Locate every P. falciparum parasite and identify its life-cycle stage.
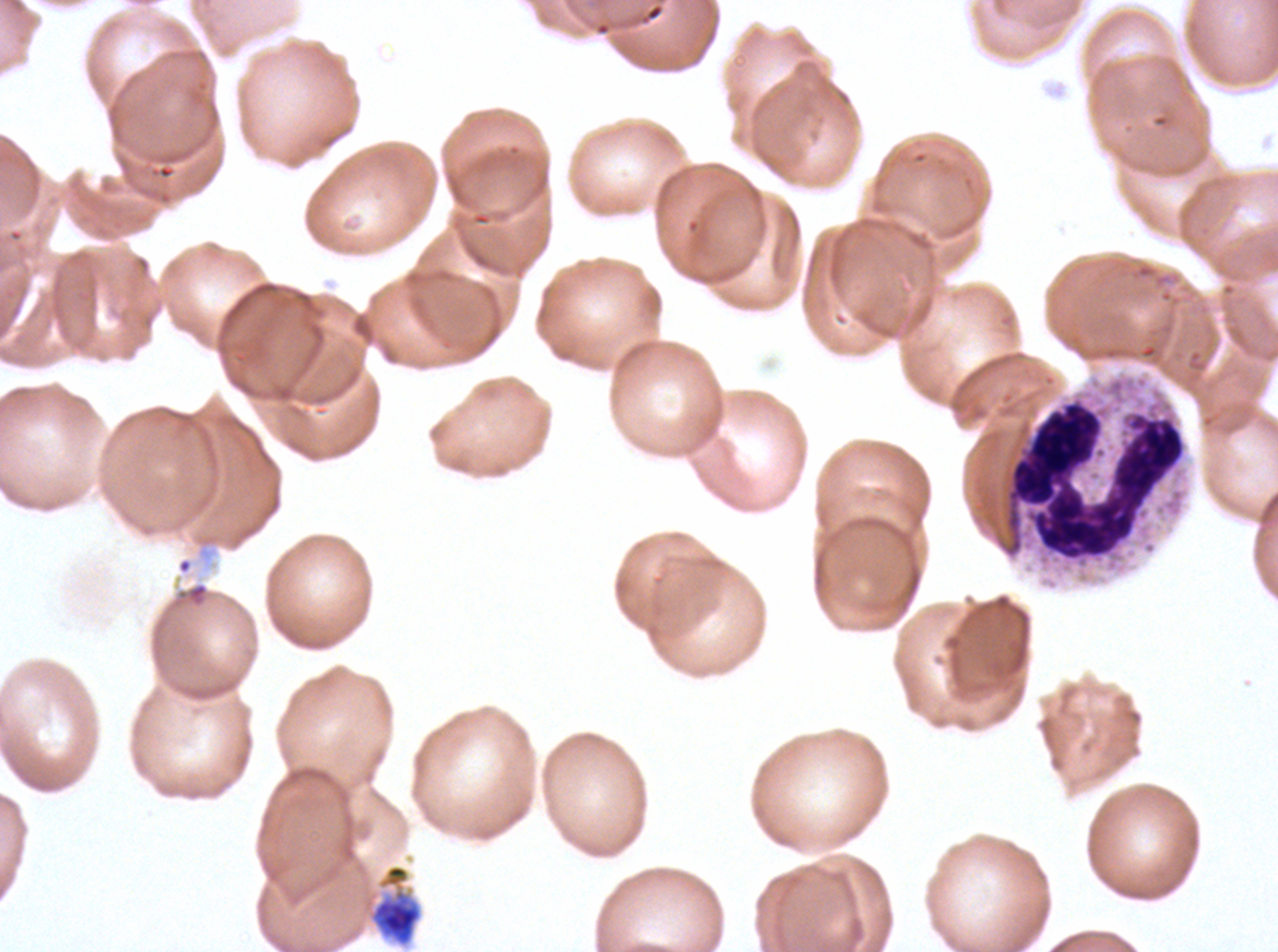
Approximate bounding rectangles given as corner coordinates in pixels from the top-left.
Early schizonts: (x1=368, y1=863, x2=423, y2=947).
No rings, late-ring/early-trophozoite forms, mid trophozoites, late trophozoites, late schizonts, segmenters, or gametocytes observed.

Summary:
  - Debris locations: (x1=1002, y1=397, x2=1186, y2=562), (x1=169, y1=580, x2=210, y2=610)
  - Specimen: P. falciparum cultured ex vivo for 24 to 48 hours, from a patient in The Gambia
  - Preparation: thin blood smear
  - Field of view: one sub-image of a larger composite
  - Stain: Giemsa
  - Image size: 1278×952 pixels